Report the malaria status of this cell.
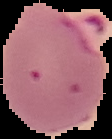

Parasitized.

Summary:
  - Image size: 112×139 pixels
  - Preparation: thin blood film
  - Image type: segmented cell region on a black background